Report the malaria status of this cell.
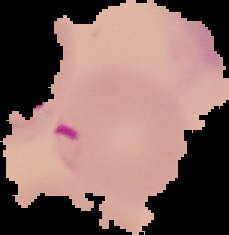
It is parasitized.

Segmented cell region on a black background. From a thin blood film. Image is 229×235 pixels.